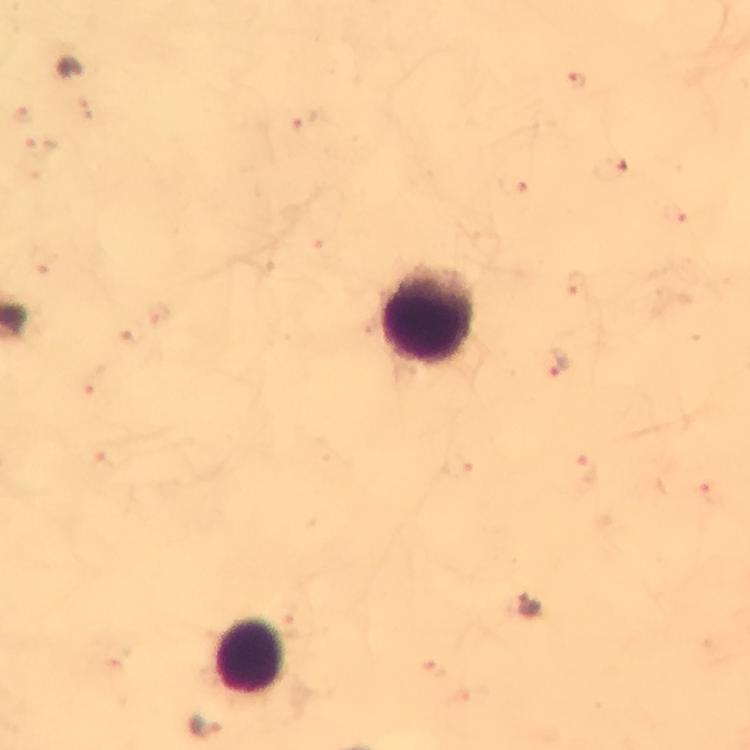

{
  "magnification": "100x",
  "capture": "smartphone mounted on the microscope",
  "context": "from a diagnostic examination for malaria",
  "immersion_oil": "applied",
  "cropped_from": "one field of view",
  "preparation": "thick blood smear",
  "image_size": "750×750 pixels",
  "malaria_parasite_locations": "approximate object centers, in pixels from the top-left corner: (x=559, y=364), (x=530, y=605), (x=204, y=725)",
  "leukocyte_locations": "approximate object centers, in pixels from the top-left corner: (x=425, y=315), (x=250, y=654)",
  "stain": "Giemsa"
}